State which parasite is depicted.
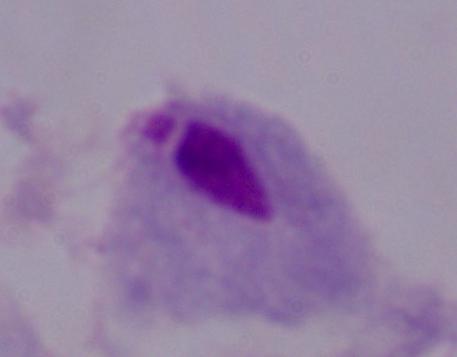

This is a trichomonad.

Summary:
  - Magnification: 1000x
  - Modality: micrograph